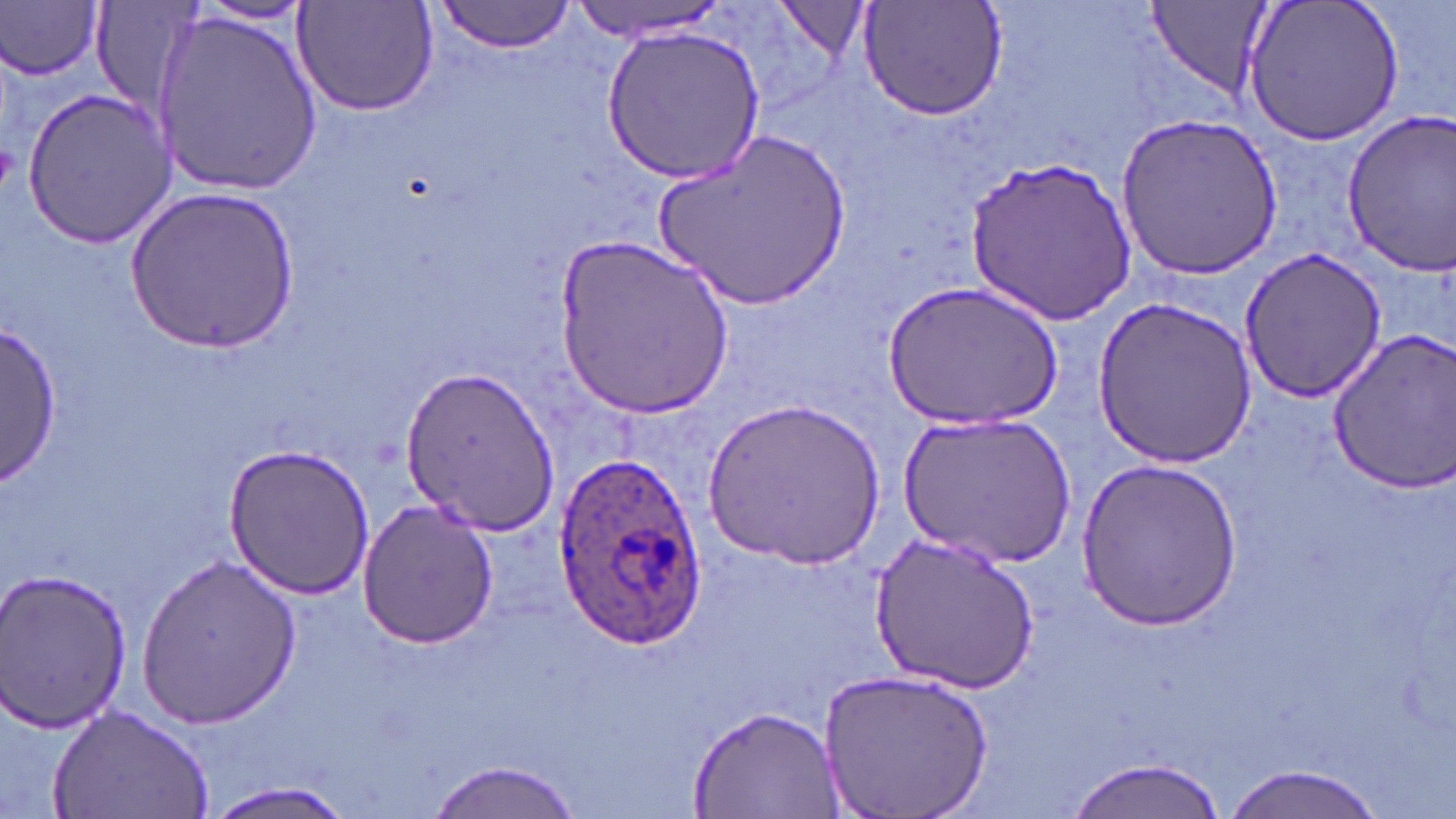
{
  "plasmodium_ovale_infected_red_blood_cell_locations": "approximate bounding boxes as [x1, y1, x2, y2] in pixels: [552, 450, 705, 652]",
  "slide_level_diagnosis": "Plasmodium ovale",
  "preparation": "thin blood film",
  "field_of_view": "single",
  "modality": "light microscopy",
  "uninfected_red_blood_cell_locations": "approximate bounding boxes as [x1, y1, x2, y2] in pixels: [569, 0, 729, 39], [776, 0, 871, 65], [1141, 0, 1276, 104], [1242, 0, 1404, 148], [3, 1, 105, 81], [193, 1, 313, 26], [293, 1, 441, 118], [432, 1, 577, 53], [858, 1, 1008, 122], [153, 10, 322, 194], [600, 24, 767, 185], [22, 86, 177, 247], [1339, 107, 1455, 278], [1115, 109, 1281, 283], [654, 128, 852, 311], [962, 154, 1137, 326], [125, 187, 298, 353], [553, 233, 735, 420], [1240, 247, 1391, 404], [884, 281, 1060, 431], [1094, 295, 1257, 467], [1, 322, 61, 478], [1325, 329, 1456, 491], [399, 361, 561, 539], [704, 395, 885, 568], [899, 411, 1075, 570], [222, 443, 375, 601], [1073, 461, 1245, 629], [356, 497, 498, 650], [871, 530, 1041, 693], [137, 552, 302, 731], [0, 571, 134, 733], [817, 667, 994, 819], [51, 703, 217, 819], [686, 703, 843, 819], [1063, 755, 1230, 819], [424, 757, 587, 819], [1218, 765, 1388, 819], [201, 780, 357, 819]",
  "magnification": "1000x",
  "stain": "May-Grünwald-Giemsa",
  "image_size": "1456×819 pixels"
}